Name the parasite shown.
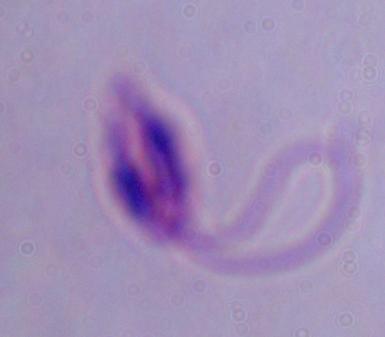
This is Leishmania.

Captured at 1000x magnification. Micrograph.